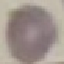
{
  "result": "no malaria parasites seen",
  "image_type": "cell patch, automatically extracted from a larger field of view and resized to 64 × 64 pixels",
  "preparation": "thin blood film",
  "capture": "smartphone camera at the microscope eyepiece",
  "stain": "Giemsa"
}